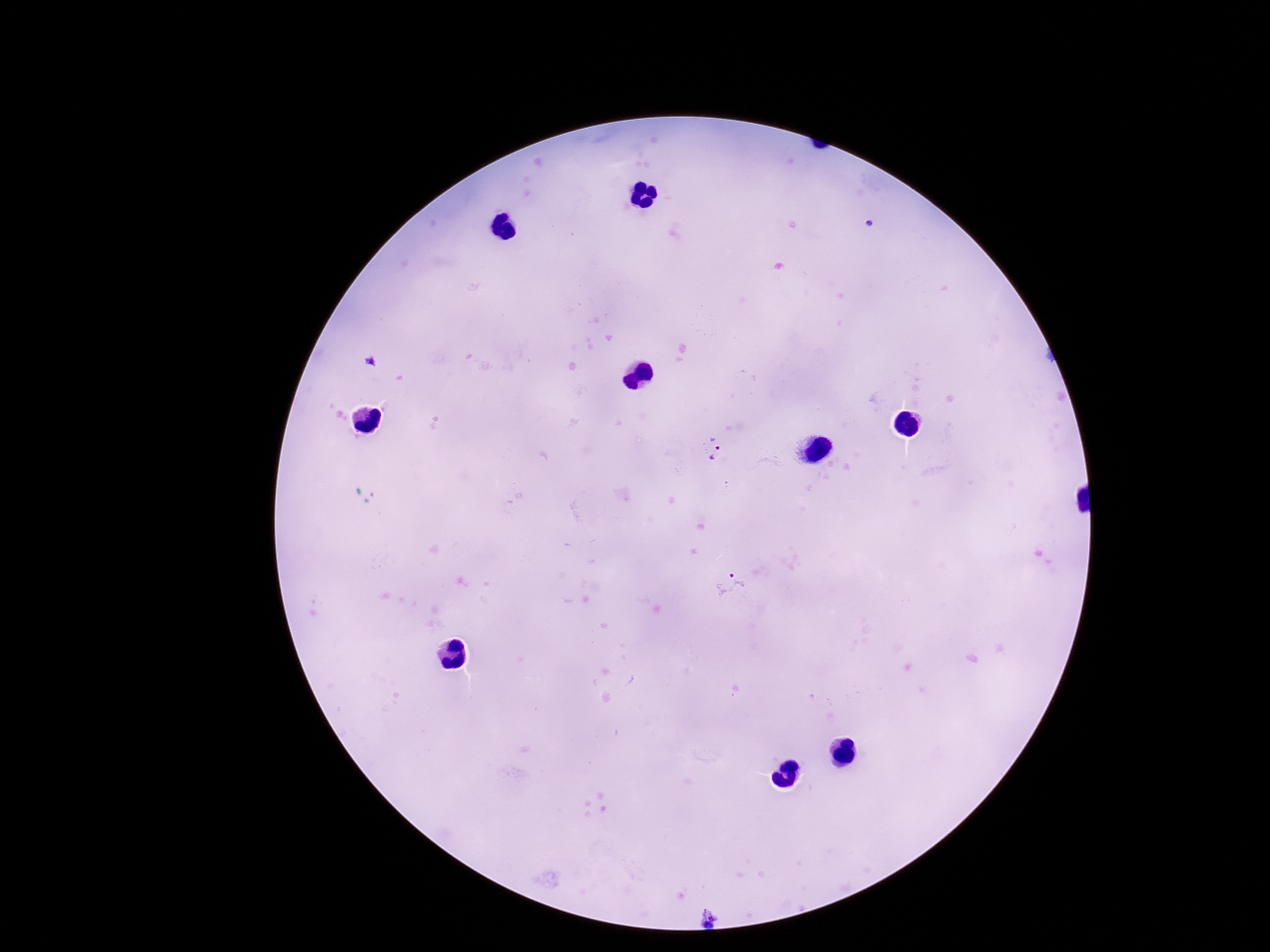

Approximate object centers, in pixels from the top-left corner. Plasmodium parasite locations: (x=711, y=447), (x=733, y=583), (x=707, y=919). Thick blood smear. Patient malaria status: infected. Image is 1270×952 pixels. One field from this slide. Smartphone photograph taken through the microscope eyepiece. Giemsa stain. 100x magnification.